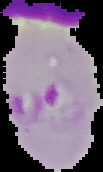
Summary:
  - Malaria status: parasitized
  - Image type: segmented cell region with the area outside set to black
  - Image size: 103×172 pixels
  - Preparation: thin blood smear